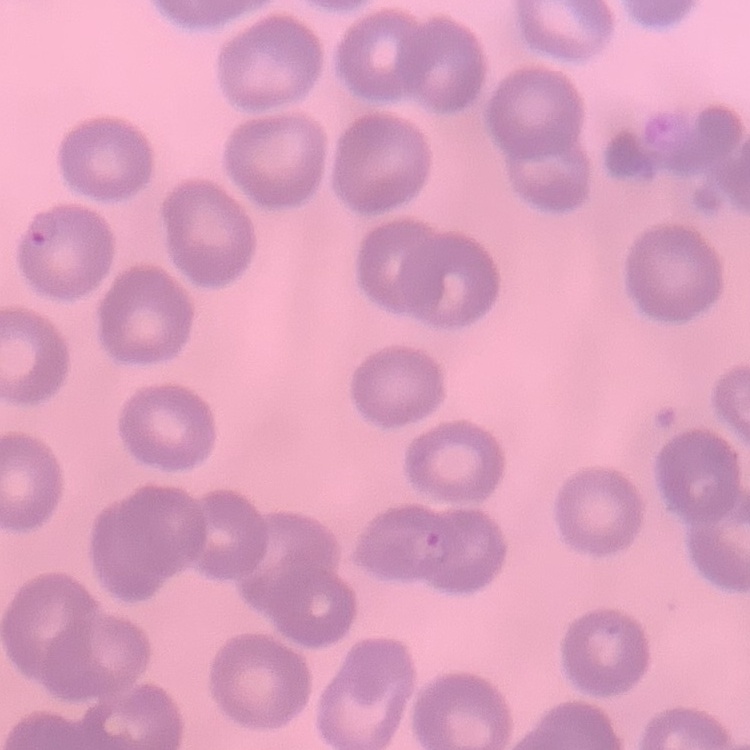

Summary:
  - Erythrocyte morphology: no rouleaux formation
  - Preparation: thin blood film
  - Image type: square crop of a larger photomicrograph
  - Stain: Field's or Giemsa